Report the malaria status of this cell.
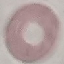

It is uninfected.

Summary:
  - Preparation: thin blood smear
  - Capture: smartphone through the microscope eyepiece
  - Stain: Giemsa
  - Image type: automatically extracted cell patch, resized to 64 × 64 pixels